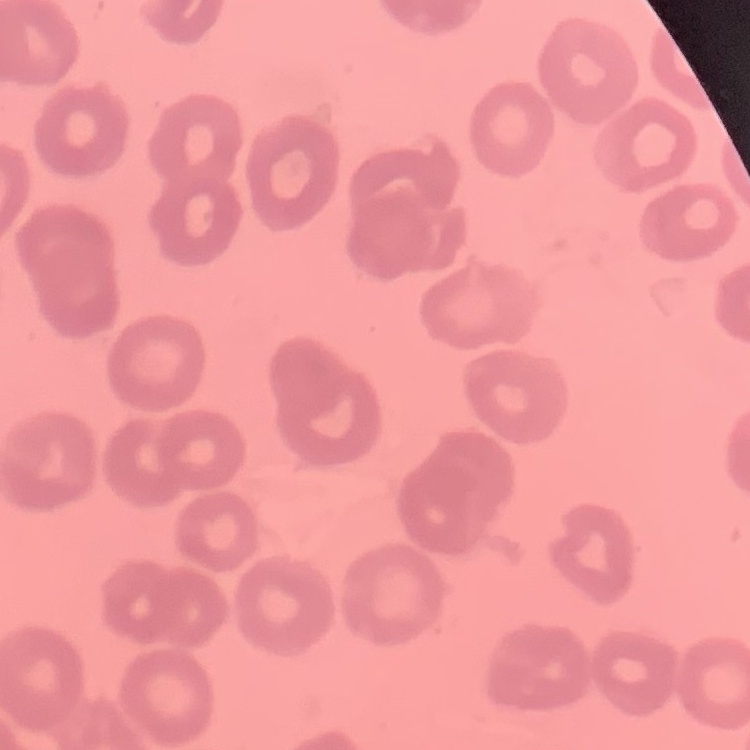

The red blood cells exhibit no rouleaux formation. Stained with either Field's or Giemsa. Square crop of a larger photomicrograph. Thin blood smear.